Locate and identify every blood parasite.
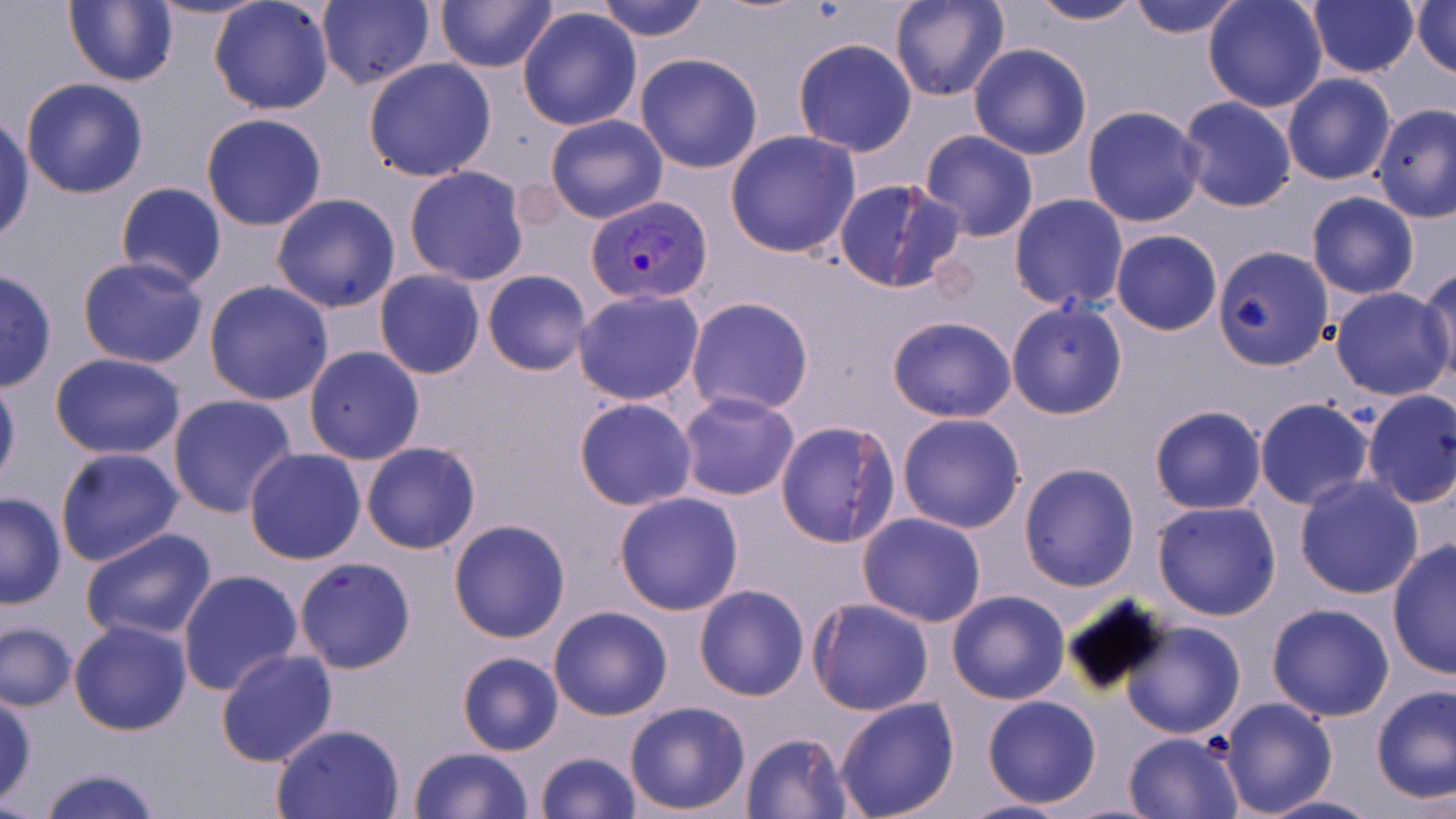

Approximate bounding boxes as (x1,y1)-(x2,y2) corner pairs in pixels.
Plasmodium vivax-infected red blood cells: (584,196)-(712,307).
No Plasmodium falciparum, Plasmodium ovale, Plasmodium malariae, Babesia divergens, or Trypanosoma brucei observed.

slide-level diagnosis = Plasmodium vivax
stain = May-Grünwald-Giemsa
magnification = 1000x
modality = light microscopy
image size = 1456×819 pixels
field of view = single
uninfected red blood cell locations = approximate bounding boxes as (x1,y1)-(x2,y2) corner pairs in pixels: (63,0)-(179,88), (147,0)-(270,22), (209,0)-(334,116), (316,0)-(434,91), (434,0)-(558,73), (597,0)-(708,42), (890,0)-(1009,103), (1025,0)-(1148,26), (1125,0)-(1246,39), (1203,0)-(1328,113), (1306,0)-(1419,78), (1411,1)-(1456,78), (517,5)-(643,131), (793,38)-(917,157), (968,43)-(1092,160), (635,54)-(764,173), (363,58)-(497,182), (1281,73)-(1396,185), (21,78)-(149,198), (1175,95)-(1299,213), (1372,104)-(1456,222), (1082,105)-(1207,228), (0,111)-(34,249), (200,112)-(327,230), (545,114)-(667,224), (725,130)-(861,259), (918,130)-(1039,241), (403,165)-(530,285), (833,178)-(964,295), (115,181)-(227,290), (1306,191)-(1419,300), (270,193)-(401,313), (1008,194)-(1128,311), (1110,229)-(1222,336), (1213,246)-(1332,371), (76,257)-(209,370), (1418,268)-(1456,390), (482,269)-(592,376), (0,270)-(58,391), (374,270)-(486,379), (204,280)-(334,405), (1330,286)-(1455,401), (574,289)-(706,405), (685,297)-(814,417), (1006,301)-(1127,419), (887,315)-(1017,422), (303,345)-(425,465), (48,352)-(188,459), (0,371)-(21,493), (1359,390)-(1456,509), (676,392)-(800,502), (167,394)-(298,518), (574,397)-(699,511), (1255,397)-(1375,511), (1149,406)-(1267,514), (1312,410)-(1438,573), (896,413)-(1025,534), (775,419)-(899,548), (360,440)-(481,555), (55,447)-(184,568), (243,448)-(366,564), (1018,462)-(1141,592), (1294,475)-(1424,600), (0,492)-(66,609), (613,492)-(744,614), (1152,500)-(1282,621), (857,512)-(986,625), (448,519)-(571,643), (79,526)-(218,643), (1387,539)-(1455,680), (293,557)-(417,674), (178,569)-(303,695), (694,585)-(809,700), (945,589)-(1071,705), (807,599)-(933,716), (1266,602)-(1395,722), (549,605)-(672,720), (68,619)-(193,736), (1123,620)-(1245,741), (1,622)-(78,712), (215,648)-(340,767), (456,651)-(564,757), (1371,684)-(1454,807), (1,692)-(37,807), (981,695)-(1102,809), (833,697)-(960,819), (1218,697)-(1337,817), (624,701)-(751,815), (270,722)-(407,818), (1124,731)-(1244,817), (740,732)-(852,818), (407,747)-(534,819), (534,751)-(643,819), (34,766)-(164,819), (1255,792)-(1384,818), (957,798)-(1071,818)
preparation = thin blood film